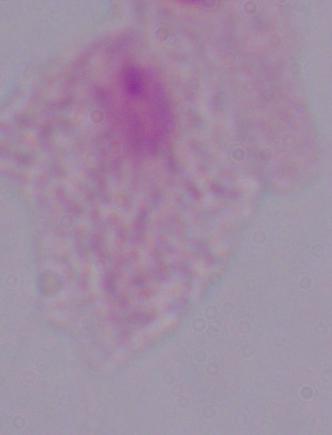
identification = trichomonad
magnification = 1000x
modality = micrograph